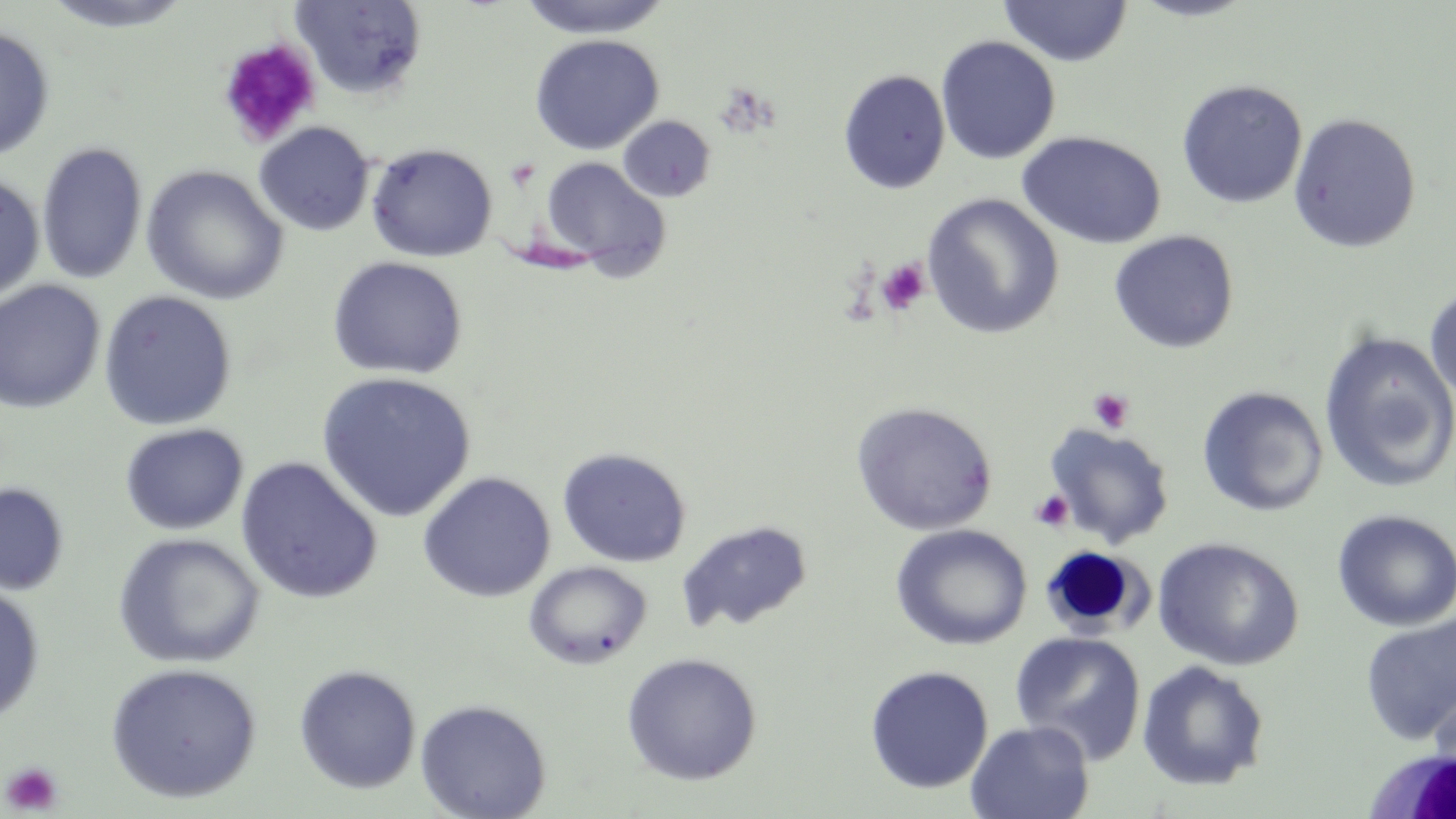

slide_level_diagnosis: negative for blood parasites
stain: May-Grünwald-Giemsa
magnification: 1000x
image_size: 1456×819 pixels
white_blood_cell_locations: 'approximate bounding boxes as named x1/y1/x2/y2 corners in pixels: (x1=1047, y1=545, x2=1163, y2=639), (x1=1362, y1=744, x2=1456, y2=818)'
modality: light microscopy
uninfected_red_blood_cell_locations: 'approximate bounding boxes as named x1/y1/x2/y2 corners in pixels: (x1=40, y1=0, x2=197, y2=33), (x1=291, y1=0, x2=428, y2=100), (x1=518, y1=0, x2=672, y2=39), (x1=1127, y1=0, x2=1260, y2=22), (x1=998, y1=1, x2=1133, y2=67), (x1=0, y1=26, x2=56, y2=161), (x1=529, y1=34, x2=665, y2=155), (x1=935, y1=35, x2=1061, y2=164), (x1=837, y1=69, x2=951, y2=194), (x1=1176, y1=79, x2=1308, y2=209), (x1=1288, y1=113, x2=1422, y2=253), (x1=618, y1=116, x2=716, y2=203), (x1=253, y1=121, x2=375, y2=237), (x1=1016, y1=130, x2=1166, y2=250), (x1=37, y1=140, x2=149, y2=285), (x1=365, y1=143, x2=498, y2=262), (x1=539, y1=156, x2=673, y2=280), (x1=141, y1=165, x2=289, y2=305), (x1=0, y1=172, x2=46, y2=303), (x1=922, y1=193, x2=1065, y2=339), (x1=1109, y1=230, x2=1239, y2=354), (x1=327, y1=256, x2=468, y2=379), (x1=0, y1=280, x2=106, y2=414), (x1=1424, y1=283, x2=1456, y2=406), (x1=98, y1=289, x2=237, y2=431), (x1=1318, y1=331, x2=1456, y2=494), (x1=316, y1=371, x2=477, y2=522), (x1=1196, y1=386, x2=1329, y2=516), (x1=850, y1=401, x2=998, y2=536), (x1=120, y1=423, x2=248, y2=535), (x1=1044, y1=424, x2=1175, y2=548), (x1=557, y1=446, x2=692, y2=568), (x1=235, y1=456, x2=384, y2=605), (x1=418, y1=471, x2=556, y2=602), (x1=0, y1=481, x2=70, y2=596), (x1=1331, y1=509, x2=1455, y2=631), (x1=677, y1=519, x2=813, y2=634), (x1=891, y1=524, x2=1032, y2=650), (x1=113, y1=533, x2=265, y2=669), (x1=1153, y1=537, x2=1304, y2=671), (x1=524, y1=561, x2=653, y2=669), (x1=0, y1=583, x2=45, y2=724), (x1=1360, y1=611, x2=1456, y2=746), (x1=1010, y1=631, x2=1146, y2=764), (x1=621, y1=652, x2=762, y2=785), (x1=1136, y1=660, x2=1270, y2=792), (x1=105, y1=662, x2=263, y2=803), (x1=293, y1=664, x2=421, y2=794), (x1=865, y1=665, x2=993, y2=794), (x1=1427, y1=678, x2=1456, y2=796), (x1=415, y1=698, x2=552, y2=819), (x1=965, y1=720, x2=1094, y2=819)'
platelet_locations: 'approximate bounding boxes as named x1/y1/x2/y2 corners in pixels: (x1=217, y1=38, x2=322, y2=149), (x1=876, y1=258, x2=930, y2=315), (x1=1088, y1=388, x2=1133, y2=433), (x1=1031, y1=490, x2=1074, y2=531), (x1=1, y1=761, x2=64, y2=815)'
field_of_view: one of a larger specimen
preparation: thin blood film